Locate every Plasmodium falciparum-infected red blood cell.
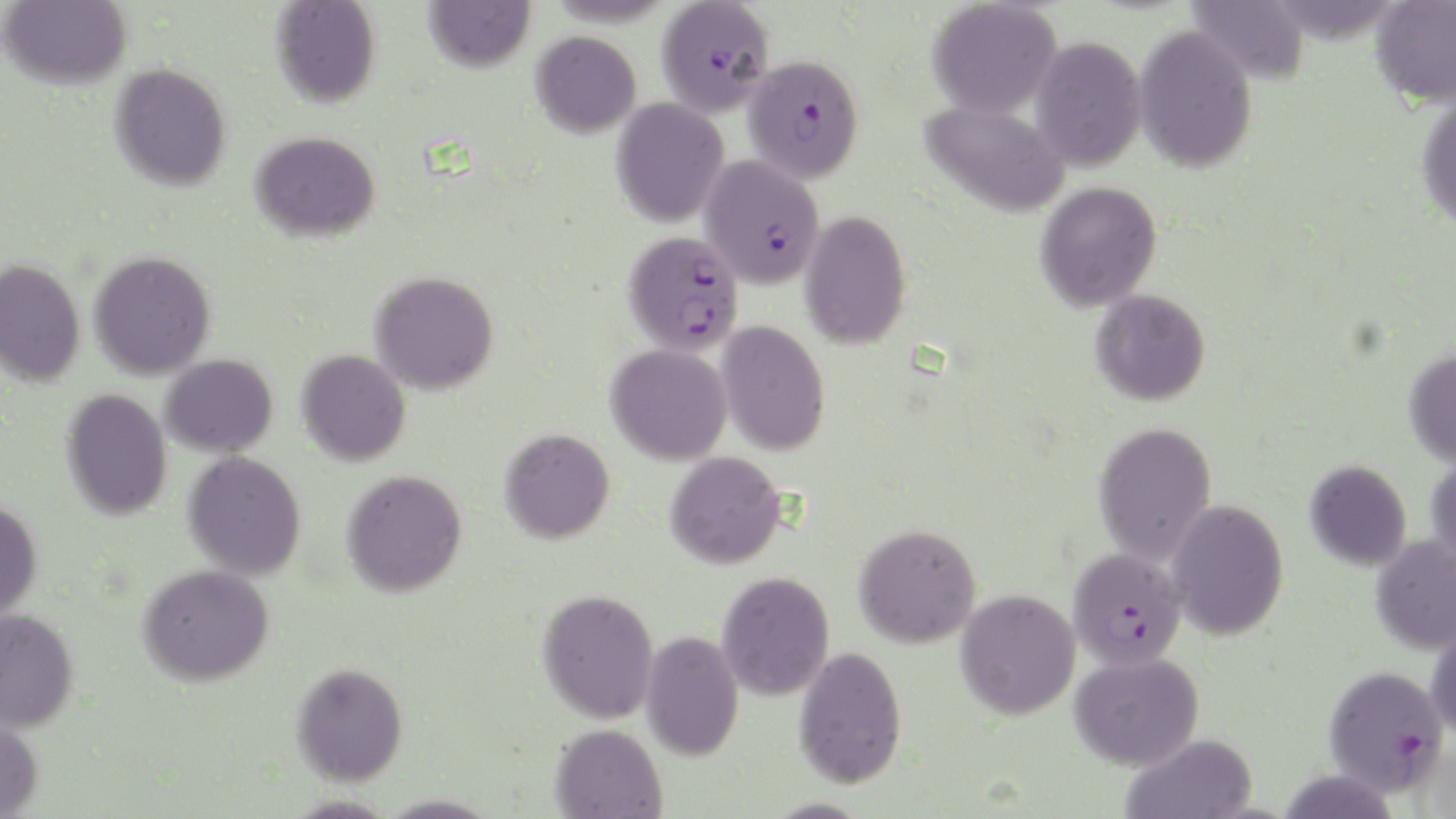

Approximate bounding boxes as [x1, y1, x2, y2] in pixels.
Plasmodium falciparum-infected red blood cells: [656, 0, 774, 116], [743, 55, 865, 183], [700, 155, 825, 289], [623, 230, 744, 355], [1067, 546, 1186, 669], [1322, 665, 1450, 798].

Summary:
  - Uninfected red blood cell locations: [423, 0, 535, 72], [1370, 0, 1456, 110], [1, 1, 132, 89], [270, 1, 381, 108], [927, 1, 1061, 118], [1186, 1, 1310, 85], [1133, 24, 1258, 173], [530, 30, 641, 138], [1030, 36, 1147, 172], [109, 63, 231, 191], [1415, 95, 1456, 233], [611, 97, 729, 228], [920, 99, 1070, 218], [250, 131, 381, 242], [1035, 181, 1162, 312], [800, 210, 911, 350], [88, 250, 216, 380], [0, 259, 85, 386], [369, 270, 499, 395], [1089, 289, 1211, 406], [716, 321, 830, 456], [606, 343, 733, 465], [296, 349, 410, 466], [1403, 349, 1456, 468], [160, 354, 278, 458], [61, 389, 172, 521], [1092, 421, 1217, 565], [499, 428, 615, 544], [183, 451, 307, 580], [665, 451, 787, 569], [1426, 454, 1456, 569], [1304, 460, 1412, 571], [341, 469, 468, 597], [0, 499, 43, 621], [1166, 499, 1290, 640], [853, 522, 981, 648], [1369, 535, 1456, 656], [139, 563, 275, 686], [717, 571, 835, 700], [537, 588, 659, 724], [955, 588, 1081, 720], [0, 608, 79, 733], [1425, 622, 1456, 742], [640, 630, 744, 761], [792, 646, 907, 789], [1069, 652, 1204, 770], [290, 662, 408, 786], [0, 714, 44, 819], [550, 723, 667, 818], [1120, 734, 1259, 819]
  - Slide-level diagnosis: Plasmodium falciparum
  - Magnification: 1000x
  - Field of view: one of a larger specimen
  - Stain: May-Grünwald-Giemsa
  - Preparation: thin blood smear
  - Image size: 1456×819 pixels
  - Modality: light microscopy